Classify this cell by malaria status.
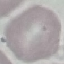
Uninfected.

Summary:
  - Image type: automatically extracted cell patch, resized to 64 × 64 pixels
  - Capture: smartphone through the microscope eyepiece
  - Preparation: thin blood film
  - Stain: Giemsa